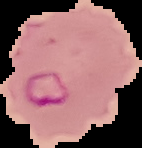 Cell region segmented out of the field of view; the surrounding area is masked to black. Image is 142×148 pixels. Result: Plasmodium parasites identified. From a thin blood film.